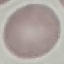 Malaria status: uninfected. Automatically extracted cell patch, resized to 64 × 64 pixels. Thin smear of blood. Photographed with a smartphone camera at the microscope eyepiece. Giemsa stain.